State which cell type is depicted.
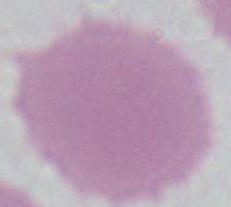

An erythrocyte.

Micrograph. Captured at 1000x magnification.